Classify this cell by malaria status.
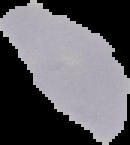

It is uninfected.

Image is 130×145 pixels. The area outside the segmented cell region is set to black. From a thin blood smear.